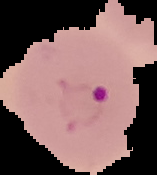 Segmented cell region on a black background. Image is 157×175 pixels. From a thin blood film. Malaria status: parasitized.